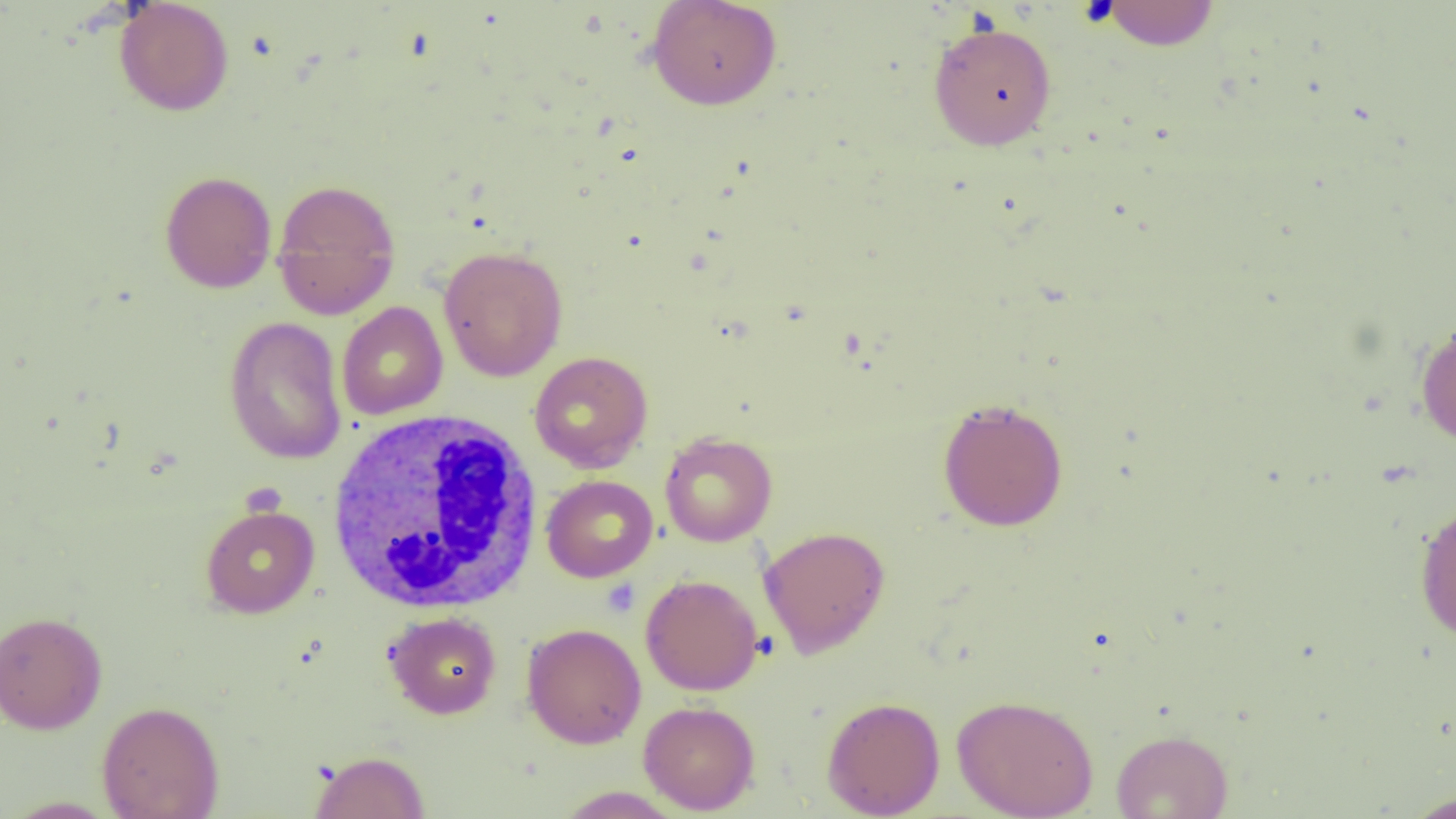

slide-level diagnosis = no evidence of blood parasites
modality = optical microscopy
preparation = thin blood smear
uninfected red blood cell locations = approximate bounding boxes as (x1, y1, x2, y2) in pixels: (646, 0, 782, 110), (113, 1, 234, 116), (1098, 1, 1220, 50), (928, 20, 1057, 150), (159, 170, 277, 293), (271, 178, 401, 320), (439, 245, 568, 382), (337, 301, 448, 420), (224, 316, 346, 465), (1415, 320, 1456, 448), (529, 351, 653, 472), (937, 397, 1069, 532), (659, 432, 777, 547), (541, 475, 658, 582), (1414, 501, 1456, 644), (200, 505, 319, 618), (758, 525, 891, 658), (640, 574, 764, 696), (0, 610, 107, 734), (383, 611, 502, 719), (521, 623, 646, 749), (951, 693, 1099, 818), (821, 696, 945, 818), (97, 700, 224, 819), (638, 701, 760, 814), (1111, 728, 1233, 819), (309, 750, 430, 819), (555, 786, 686, 818), (1402, 790, 1456, 818), (3, 796, 120, 818)
platelet locations = approximate bounding boxes as (x1, y1, x2, y2) in pixels: (601, 579, 640, 617)
magnification = 1000x
white blood cell locations = approximate bounding boxes as (x1, y1, x2, y2) in pixels: (324, 408, 546, 615)
field of view = single
image size = 1456×819 pixels